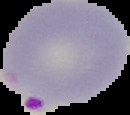

Summary:
  - Image size: 130×115 pixels
  - Image type: segmented cell region on a black background
  - Malaria status: parasitized
  - Preparation: thin blood smear